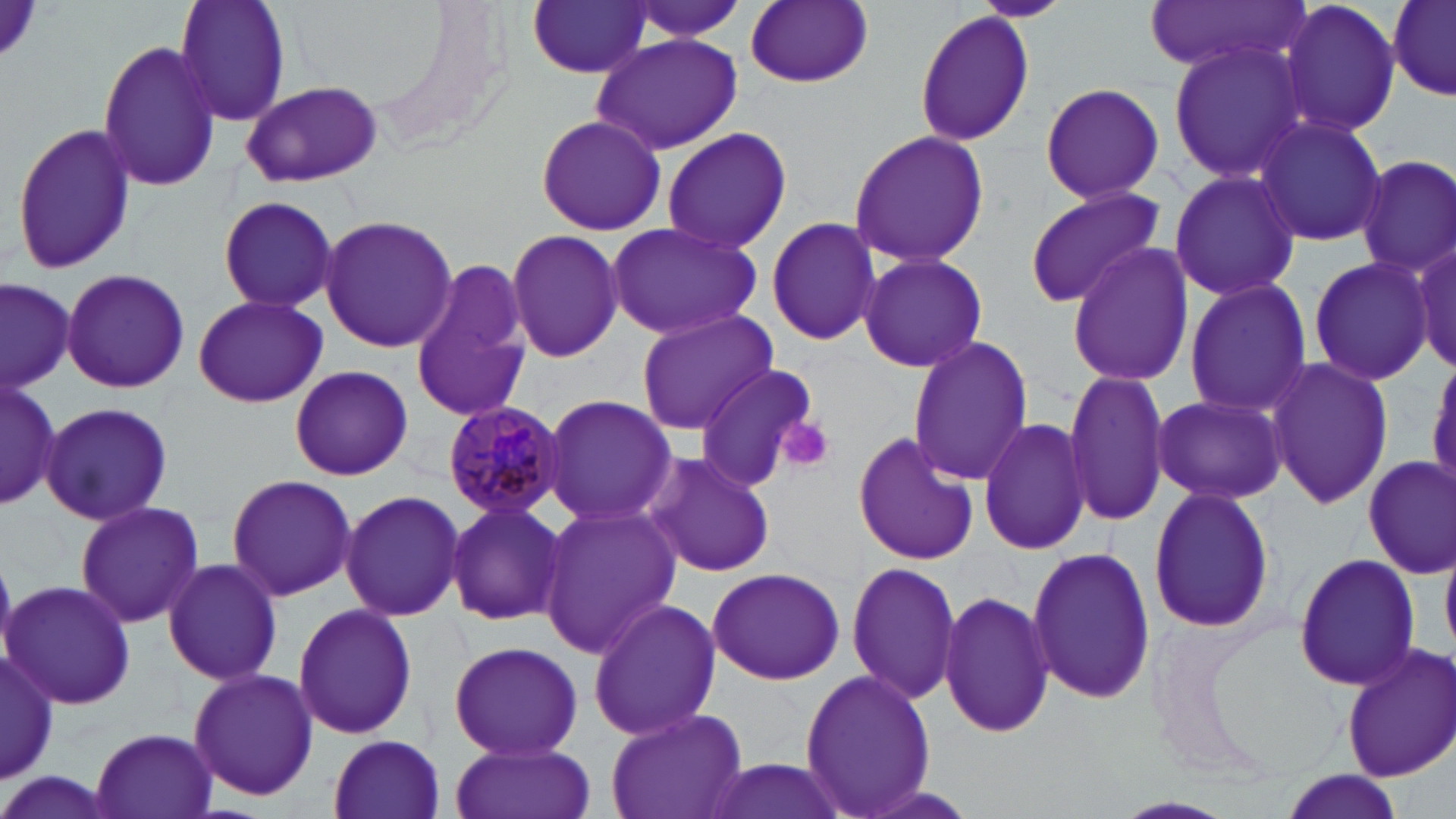

Summary:
  - Coordinate format: approximate bounding boxes as (x1, y1, x2, y2) in pixels
  - Platelet locations: (778, 417, 836, 471)
  - Uninfected red blood cell locations: (172, 0, 292, 126), (619, 0, 751, 41), (972, 0, 1073, 23), (1145, 0, 1308, 74), (1278, 0, 1402, 141), (1387, 0, 1456, 103), (527, 1, 652, 79), (743, 1, 874, 88), (914, 10, 1036, 148), (590, 32, 743, 156), (97, 40, 223, 191), (1166, 40, 1315, 184), (240, 79, 384, 189), (1038, 82, 1167, 204), (536, 114, 666, 237), (1251, 115, 1388, 247), (9, 119, 136, 276), (658, 126, 793, 254), (847, 130, 993, 268), (1354, 153, 1456, 278), (1167, 170, 1303, 302), (1023, 185, 1167, 309), (214, 194, 340, 312), (765, 213, 883, 347), (319, 215, 458, 354), (604, 222, 762, 341), (506, 229, 625, 362), (1413, 240, 1454, 375), (1066, 243, 1195, 387), (856, 252, 988, 374), (1307, 254, 1435, 388), (407, 263, 535, 420), (60, 267, 190, 394), (0, 276, 75, 388), (1183, 278, 1313, 418), (191, 294, 329, 409), (635, 309, 779, 432), (907, 335, 1033, 486), (1266, 356, 1393, 510), (692, 362, 825, 493), (288, 364, 414, 481), (1063, 369, 1170, 524), (0, 377, 63, 512), (540, 393, 675, 529), (1151, 393, 1287, 504), (40, 400, 175, 527), (978, 417, 1092, 556), (852, 431, 980, 566), (643, 450, 776, 578), (1361, 453, 1455, 577), (225, 473, 357, 602), (1148, 488, 1276, 633), (339, 490, 466, 621), (75, 499, 204, 629), (443, 499, 569, 626), (537, 503, 681, 658), (1027, 548, 1157, 704), (1291, 552, 1423, 691), (163, 557, 284, 686), (845, 562, 962, 704), (705, 566, 846, 685), (3, 576, 137, 710), (939, 590, 1055, 740), (587, 599, 724, 739), (292, 603, 420, 741), (447, 640, 585, 759), (1338, 643, 1456, 783), (1, 649, 57, 785), (798, 667, 938, 818), (187, 668, 318, 799), (605, 704, 749, 819), (89, 728, 219, 819), (328, 734, 447, 818), (448, 741, 594, 819), (701, 757, 848, 819), (0, 770, 114, 819), (1277, 771, 1402, 818)
  - Plasmodium malariae-infected red blood cell locations: (442, 398, 567, 523)
  - Slide-level diagnosis: Plasmodium malariae
  - Image size: 1456×819 pixels
  - Stain: May-Grünwald-Giemsa
  - Modality: optical microscopy
  - Preparation: thin blood film
  - Field of view: one of a larger specimen
  - Magnification: 1000x